Identify the blood parasite species.
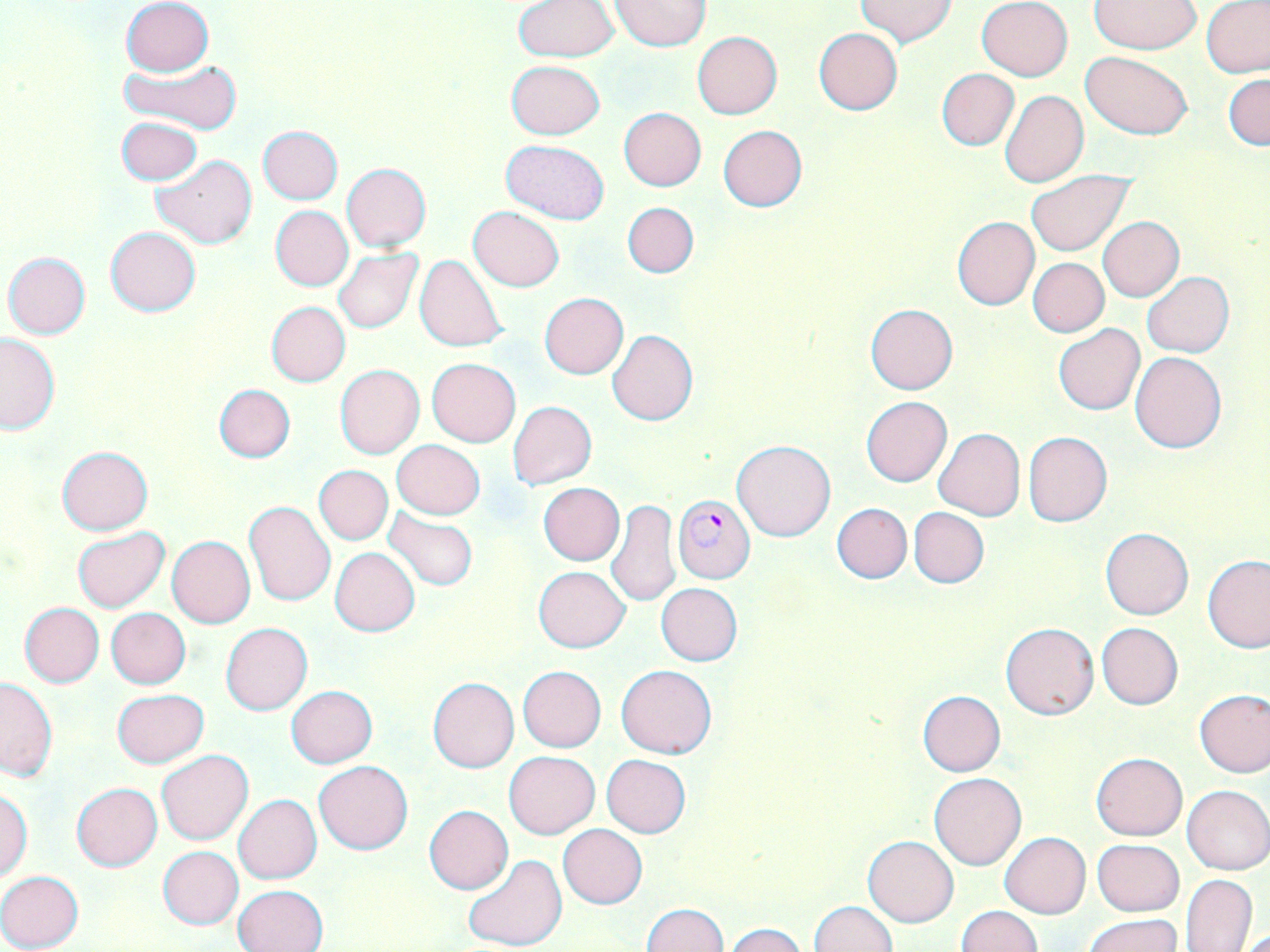

Plasmodium falciparum.

modality = optical microscopy
magnification = 1000x
field of view = single
stain = May-Grünwald-Giemsa
uninfected red blood cell locations = approximate bounding boxes as (x1,y1)-(x2,y2) corner pairs in pixels: (609,0)-(709,50), (977,0)-(1073,80), (121,1)-(214,76), (512,1)-(619,60), (855,1)-(955,47), (1090,1)-(1201,53), (1200,2)-(1270,79), (1092,4)-(1198,109), (813,27)-(903,115), (692,31)-(782,119), (1080,51)-(1193,138), (121,58)-(241,133), (506,59)-(604,139), (937,68)-(1019,151), (1224,72)-(1269,152), (1000,90)-(1089,188), (618,107)-(706,191), (116,117)-(203,185), (258,126)-(342,204), (718,126)-(808,213), (501,140)-(608,225), (151,156)-(256,248), (341,163)-(430,251), (1026,170)-(1133,256), (623,202)-(698,278), (271,206)-(353,291), (468,207)-(564,291), (951,216)-(1040,311), (1098,216)-(1184,301), (106,227)-(200,316), (334,248)-(422,333), (3,253)-(90,339), (415,255)-(508,353), (1028,258)-(1109,336), (1141,273)-(1233,357), (539,293)-(628,379), (265,301)-(350,387), (865,303)-(957,393), (1053,324)-(1145,415), (608,330)-(698,425), (0,333)-(61,435), (1130,352)-(1227,453), (427,358)-(521,447), (334,364)-(425,458), (214,384)-(295,462), (861,396)-(952,487), (507,401)-(597,489), (933,428)-(1025,520), (1024,431)-(1113,527), (392,440)-(485,518), (733,440)-(836,541), (56,446)-(154,535), (315,466)-(392,544), (538,483)-(624,565), (605,499)-(681,606), (244,501)-(335,606), (832,503)-(911,584), (383,507)-(479,593), (908,507)-(988,588), (1100,527)-(1193,621), (71,528)-(170,612), (167,536)-(255,629), (330,548)-(421,636), (1203,554)-(1270,654), (535,566)-(629,652), (655,583)-(743,666), (18,603)-(104,688), (106,608)-(190,689), (1001,621)-(1099,719), (221,623)-(312,715), (1096,623)-(1183,709), (616,664)-(716,758), (518,666)-(606,752), (0,677)-(57,781), (428,678)-(519,773), (286,686)-(377,768), (1195,688)-(1270,778), (112,689)-(208,768), (917,690)-(1006,776), (156,749)-(254,845), (505,751)-(598,838), (1092,753)-(1187,840), (602,754)-(690,837), (314,760)-(413,854), (930,772)-(1027,870), (71,783)-(162,871), (1182,784)-(1270,874), (0,790)-(32,879), (233,794)-(322,884), (424,805)-(512,894), (558,825)-(647,909), (1000,833)-(1090,918), (863,835)-(958,927), (1093,838)-(1183,916), (158,847)-(243,929), (463,854)-(569,950), (0,870)-(84,950), (1178,873)-(1257,952), (233,884)-(328,952), (808,900)-(897,952), (640,903)-(729,952), (956,905)-(1042,952), (1084,913)-(1184,952), (724,923)-(806,951)
image size = 1270×952 pixels
preparation = thin blood film
Plasmodium falciparum-infected red blood cell locations = approximate bounding boxes as (x1,y1)-(x2,y2) corner pairs in pixels: (672,495)-(755,583)